State which parasite is depicted.
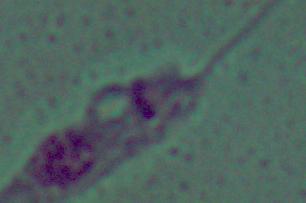

Leishmania.

magnification = 1000x
modality = micrograph